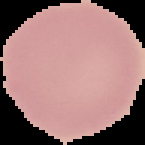

Image is 145×145 pixels. Malaria status: uninfected. Cell region segmented out of the field of view; the surrounding area is masked to black. From a thin blood film.